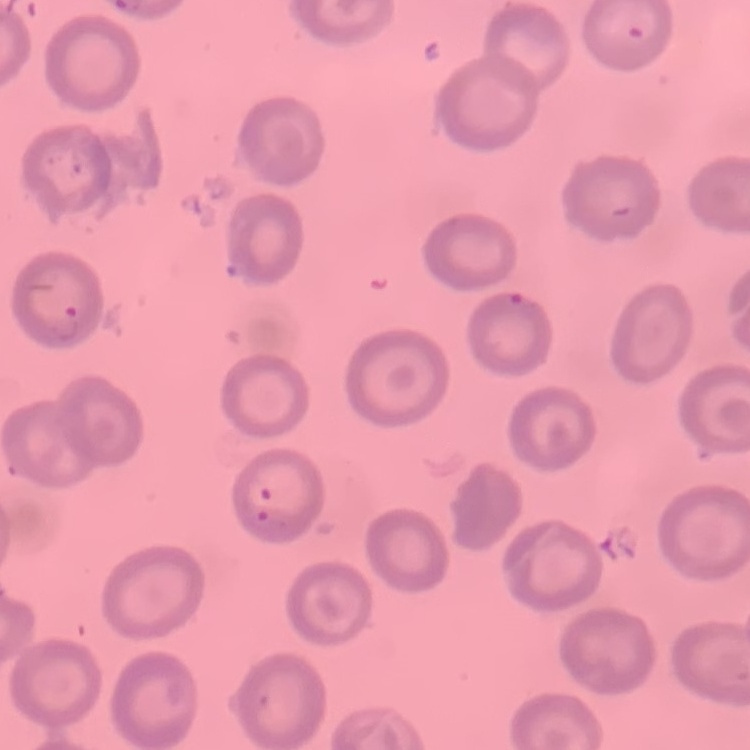

Summary:
  - Erythrocyte morphology: no rouleaux formation
  - Preparation: thin blood film
  - Stain: Field's or Giemsa
  - Image type: one tile cut from a larger photomicrograph